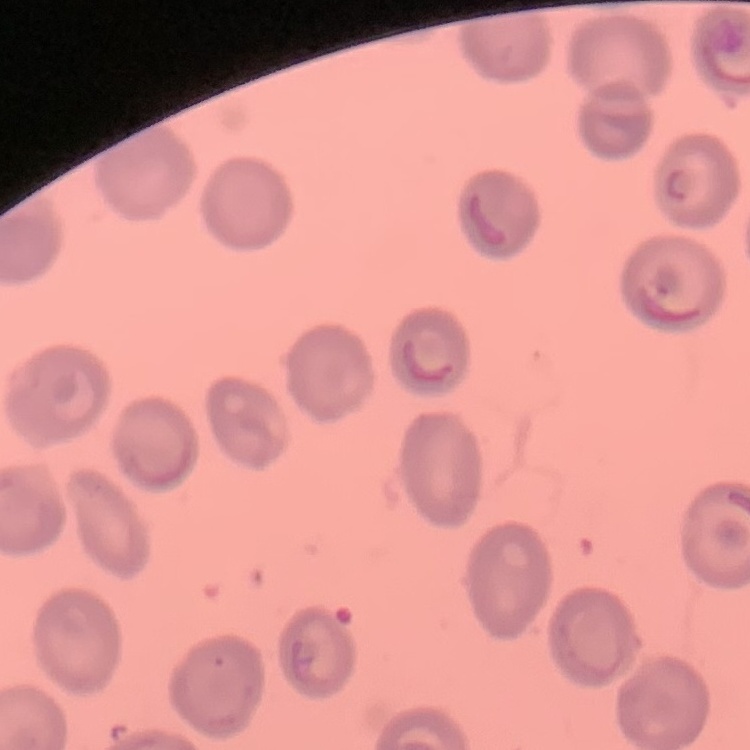

Summary:
  - Erythrocyte morphology: no rouleaux formation
  - Stain: Field's or Giemsa
  - Image type: one tile cut from a larger photomicrograph
  - Preparation: thin blood smear